Report the malaria status of this cell.
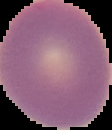

It is uninfected.

Image is 112×130 pixels. From a thin blood film. Cell region segmented out of the field of view; the surrounding area is masked to black.